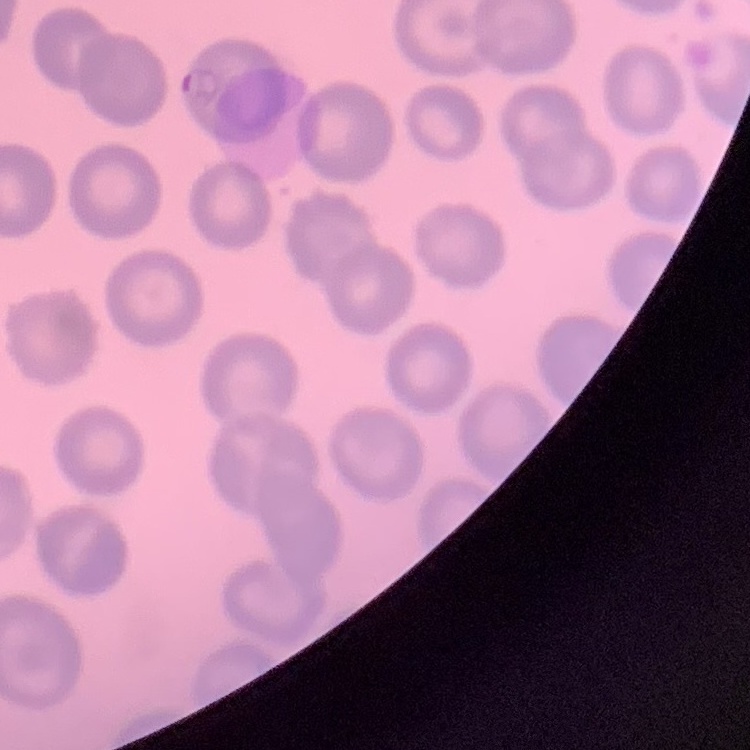 The erythrocytes show no rouleaux formation. Stained with either Field's or Giemsa. Square crop of a larger photomicrograph. Thin blood smear.